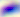
{
  "magnification": "400x",
  "identification": "Toxoplasma gondii",
  "modality": "micrograph"
}